Identify the blood parasite species.
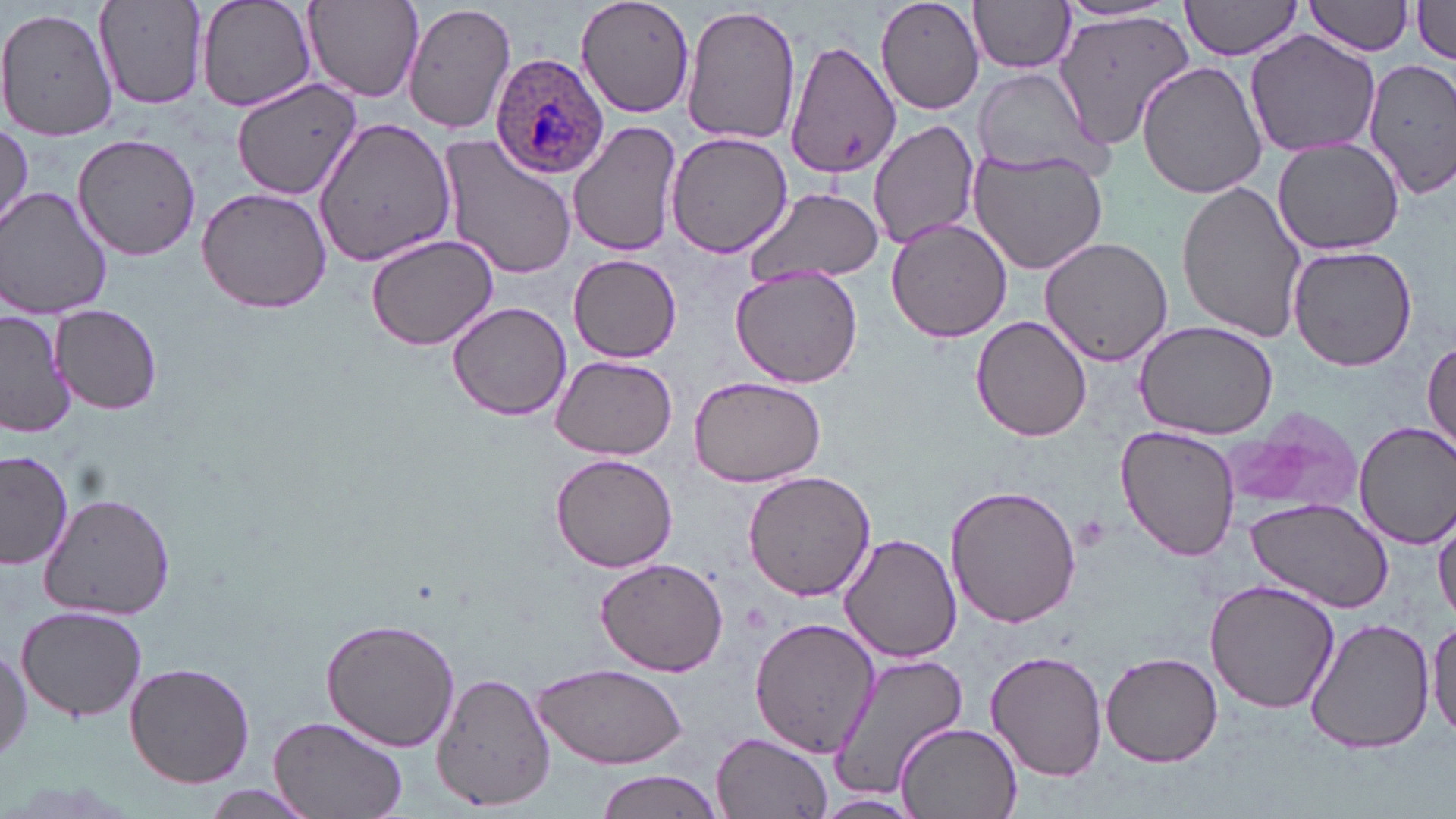
Plasmodium ovale.

stain = May-Grünwald-Giemsa
magnification = 1000x
uninfected red blood cell locations = approximate bounding boxes as [x1, y1, x2, y2] in pixels: [93, 0, 210, 111], [195, 0, 318, 115], [302, 0, 425, 102], [403, 0, 517, 135], [572, 0, 696, 118], [875, 0, 985, 114], [1180, 0, 1306, 61], [1306, 0, 1414, 56], [969, 1, 1078, 75], [1410, 1, 1456, 62], [1056, 2, 1183, 26], [681, 3, 800, 148], [2, 6, 117, 140], [1054, 13, 1192, 155], [1245, 29, 1382, 158], [783, 38, 903, 177], [1363, 56, 1456, 200], [1137, 59, 1268, 200], [971, 67, 1104, 178], [232, 79, 364, 200], [314, 116, 457, 267], [867, 118, 980, 247], [569, 121, 683, 259], [0, 123, 31, 237], [665, 131, 796, 258], [72, 134, 201, 260], [437, 136, 579, 282], [1270, 137, 1405, 256], [967, 146, 1108, 276], [1176, 178, 1312, 342], [1, 186, 115, 319], [741, 186, 883, 288], [196, 187, 335, 316], [886, 218, 1013, 344], [364, 233, 499, 351], [1038, 236, 1174, 367], [1287, 244, 1418, 372], [568, 254, 683, 362], [729, 264, 863, 389], [447, 301, 573, 420], [53, 304, 161, 415], [0, 311, 72, 439], [970, 315, 1093, 442], [1132, 318, 1279, 440], [1422, 337, 1456, 461], [547, 354, 677, 457], [688, 375, 828, 490], [1223, 411, 1360, 517], [1354, 421, 1456, 549], [1115, 426, 1241, 561], [0, 450, 76, 572], [551, 455, 677, 572], [741, 469, 879, 600], [946, 484, 1080, 628], [40, 492, 176, 619], [1242, 496, 1395, 614], [1432, 509, 1456, 624], [839, 534, 961, 662], [597, 557, 728, 676], [1205, 579, 1339, 715], [16, 606, 148, 721], [1427, 614, 1456, 741], [1305, 616, 1434, 755], [751, 617, 880, 758], [322, 618, 461, 753], [0, 638, 30, 767], [987, 649, 1107, 780], [830, 651, 965, 801], [1100, 651, 1223, 767], [123, 661, 256, 789], [534, 662, 689, 770], [434, 673, 555, 809], [267, 714, 409, 819], [892, 721, 1022, 818], [710, 732, 836, 819], [595, 770, 723, 819], [201, 786, 319, 818], [814, 792, 921, 816]
Plasmodium ovale-infected red blood cell locations = approximate bounding boxes as [x1, y1, x2, y2] in pixels: [490, 52, 610, 179]
image size = 1456×819 pixels
platelet locations = approximate bounding boxes as [x1, y1, x2, y2] in pixels: [1074, 514, 1112, 553]
preparation = thin blood smear
modality = light microscopy
field of view = single